Report the malaria status of this cell.
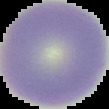

Uninfected.

Summary:
  - Image size: 109×109 pixels
  - Preparation: thin blood film
  - Image type: segmented cell region with the area outside set to black